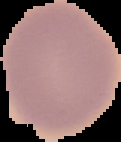

Summary:
  - Image size: 121×142 pixels
  - Image type: cell region segmented out of the field of view; surrounding area masked to black
  - Malaria status: uninfected
  - Preparation: thin blood film